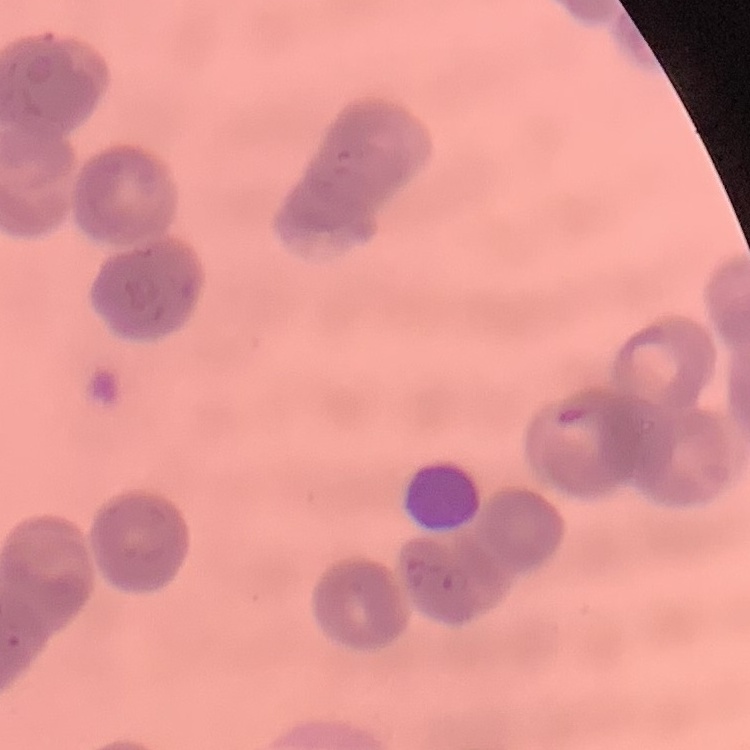
red_blood_cell_morphology: rouleaux formation
image_type: one tile cut from a larger photomicrograph
stain: Field's or Giemsa
preparation: thin blood film